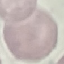

Result: negative for malaria parasites. Thin smear of blood. Giemsa-stained preparation. Photographed with a smartphone camera at the microscope eyepiece. Cell patch, automatically extracted from a larger field of view and resized to 64 × 64 pixels.